Comment on the morphology of the erythrocytes.
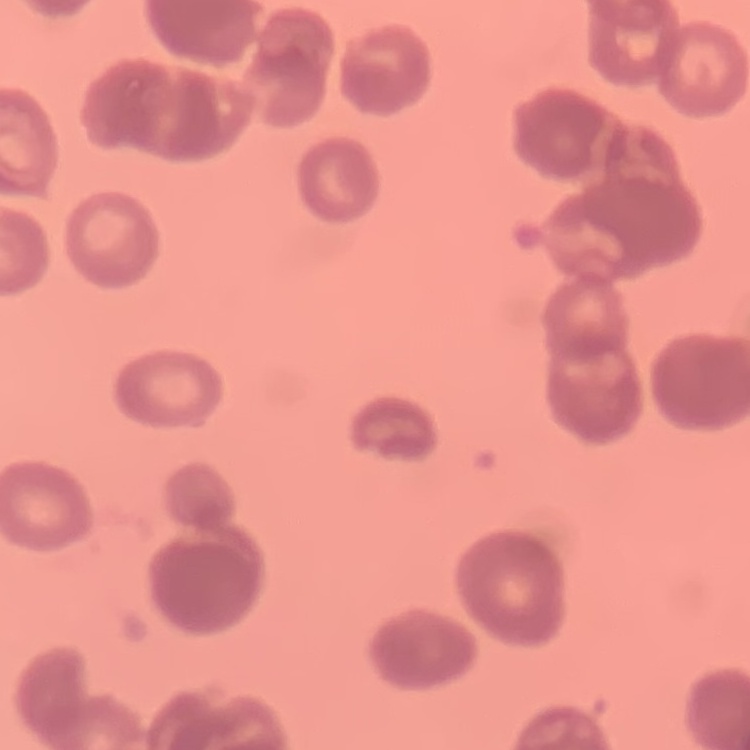
They show rouleaux formation.

preparation = thin blood smear
image type = square crop of a larger photomicrograph
stain = Field's or Giemsa